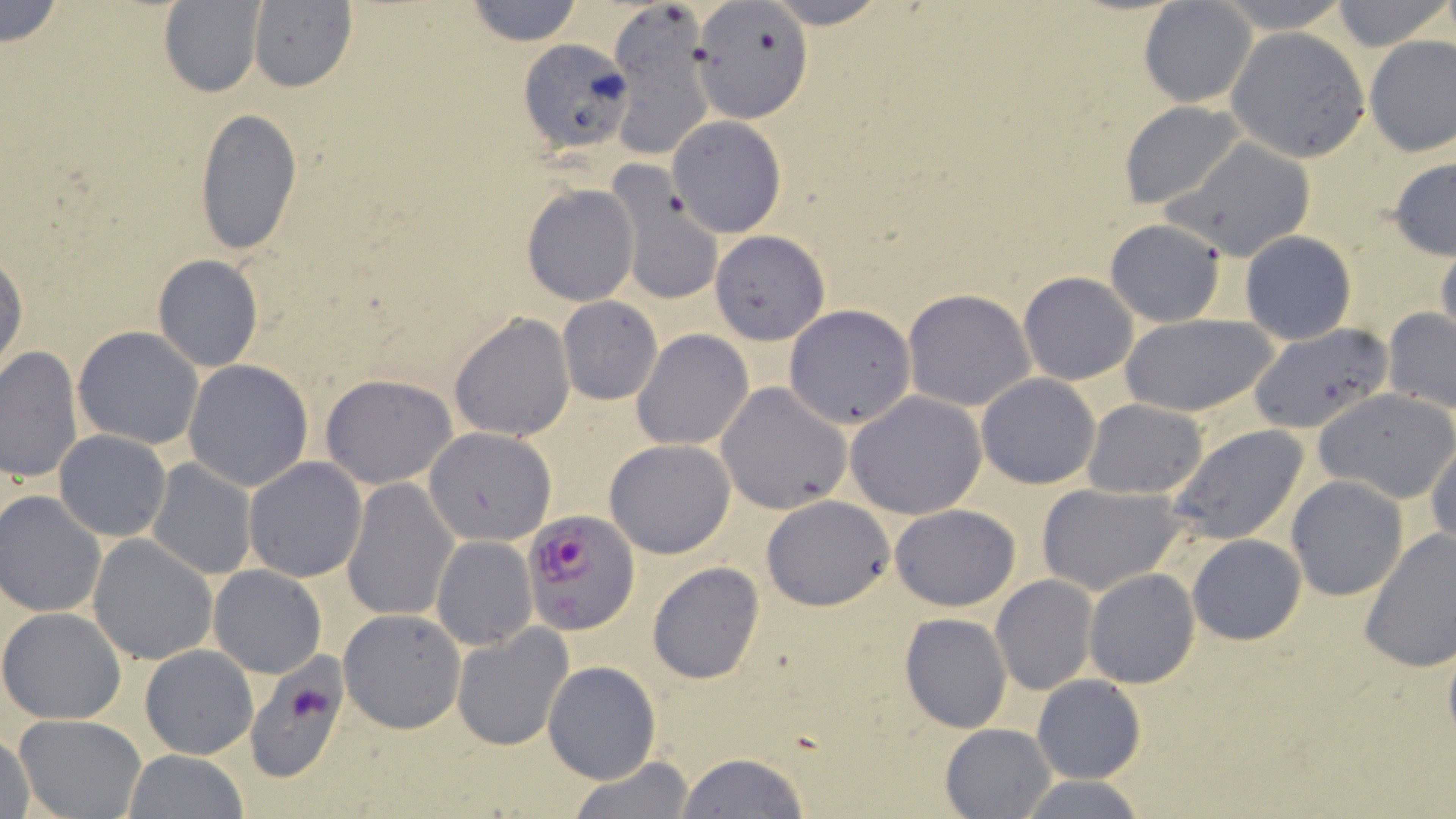
Approximate bounding boxes as [x1, y1, x2, y2] in pixels. Uninfected red blood cell locations: [1, 0, 64, 49], [463, 0, 583, 46], [758, 0, 893, 29], [1210, 0, 1355, 33], [1329, 0, 1452, 51], [246, 1, 356, 93], [1137, 1, 1258, 107], [159, 2, 265, 97], [695, 3, 810, 121], [606, 7, 712, 160], [1226, 28, 1369, 162], [1364, 34, 1456, 157], [517, 38, 632, 156], [1120, 101, 1247, 208], [193, 106, 302, 256], [667, 115, 786, 238], [1160, 136, 1317, 261], [1387, 156, 1455, 262], [613, 179, 722, 307], [521, 183, 639, 307], [1105, 217, 1228, 327], [709, 229, 830, 344], [1239, 231, 1357, 345], [1435, 243, 1456, 350], [0, 251, 28, 380], [152, 254, 263, 371], [1017, 272, 1139, 386], [902, 288, 1034, 411], [556, 297, 662, 405], [785, 304, 916, 428], [1382, 307, 1456, 415], [449, 312, 576, 442], [1118, 312, 1281, 419], [1245, 323, 1391, 434], [73, 326, 204, 449], [631, 329, 754, 451], [0, 346, 83, 483], [184, 359, 314, 490], [320, 373, 459, 488], [975, 374, 1101, 489], [717, 382, 852, 515], [1316, 387, 1456, 503], [845, 391, 990, 519], [1083, 399, 1209, 499], [424, 424, 556, 545], [1168, 424, 1311, 546], [54, 430, 171, 542], [1427, 435, 1456, 552], [605, 438, 736, 559], [244, 456, 368, 581], [145, 458, 257, 580], [340, 476, 459, 621], [1286, 476, 1408, 601], [1036, 483, 1187, 596], [1, 492, 105, 617], [761, 494, 895, 610], [888, 503, 1020, 612], [1359, 530, 1456, 672], [87, 534, 219, 665], [1187, 534, 1307, 644], [432, 536, 536, 650], [646, 563, 765, 684], [207, 565, 326, 678], [1084, 568, 1200, 688], [991, 576, 1098, 694], [0, 607, 127, 725], [338, 608, 467, 733], [898, 612, 1013, 734], [451, 622, 574, 752], [140, 644, 257, 760], [243, 656, 352, 784], [542, 661, 661, 784], [1032, 675, 1145, 784], [14, 714, 147, 819], [939, 723, 1055, 817], [1, 727, 37, 819], [124, 751, 247, 817], [676, 752, 810, 818], [568, 756, 696, 819], [1013, 774, 1151, 818]. Plasmodium falciparum-infected red blood cell locations: [523, 509, 640, 634]. Slide-level diagnosis: Plasmodium falciparum. One field of a larger specimen. Thin blood smear. Image is 1456×819 pixels. Optical microscopy. 1000x magnification. May-Grünwald-Giemsa-stained preparation.